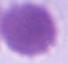
{
  "modality": "micrograph",
  "identification": "red blood cell",
  "magnification": "1000x"
}